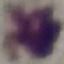

Malaria status: uninfected. Thin smear of blood. Giemsa stain. Photographed with a smartphone camera at the microscope eyepiece. Automatically extracted cell patch, resized to 64 × 64 pixels.